State which parasite is depicted.
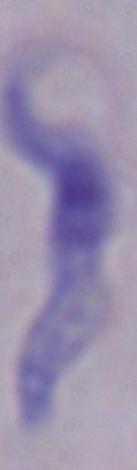
This is a trypanosome.

Captured at 1000x magnification. Micrograph.